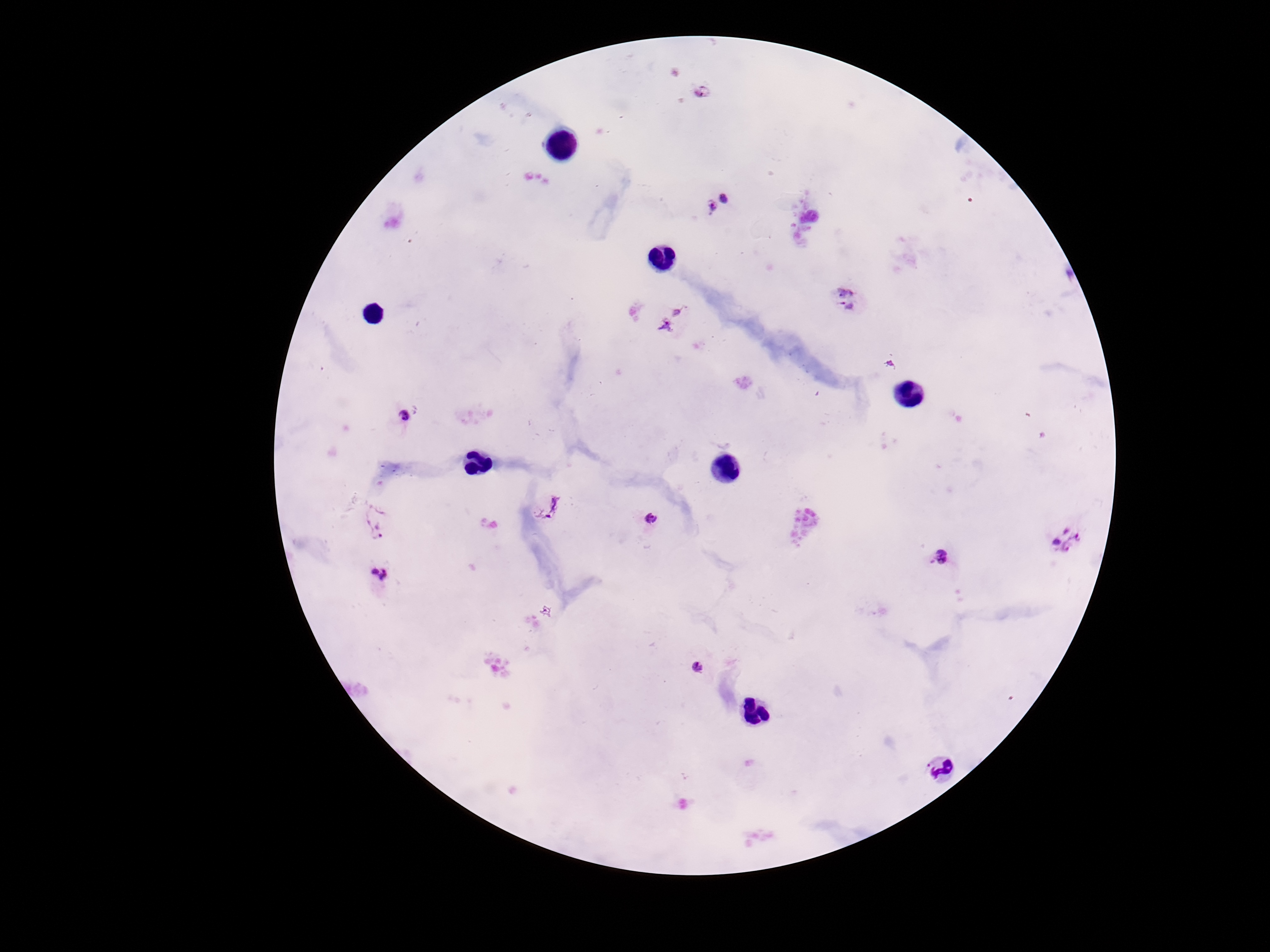

Approximate centers as {x, y} in pixels.
Summary:
  - Plasmodium parasite locations: {722, 205}, {846, 298}, {672, 318}, {404, 415}, {552, 509}, {652, 520}, {378, 521}, {1068, 539}, {940, 555}, {382, 575}, {698, 667}
  - Stain: Giemsa
  - Patient malaria status: positive
  - Magnification: 100x
  - Preparation: thick peripheral-blood smear
  - Image size: 1270×952 pixels
  - Field of view: one from this slide
  - Capture: smartphone camera through the microscope eyepiece